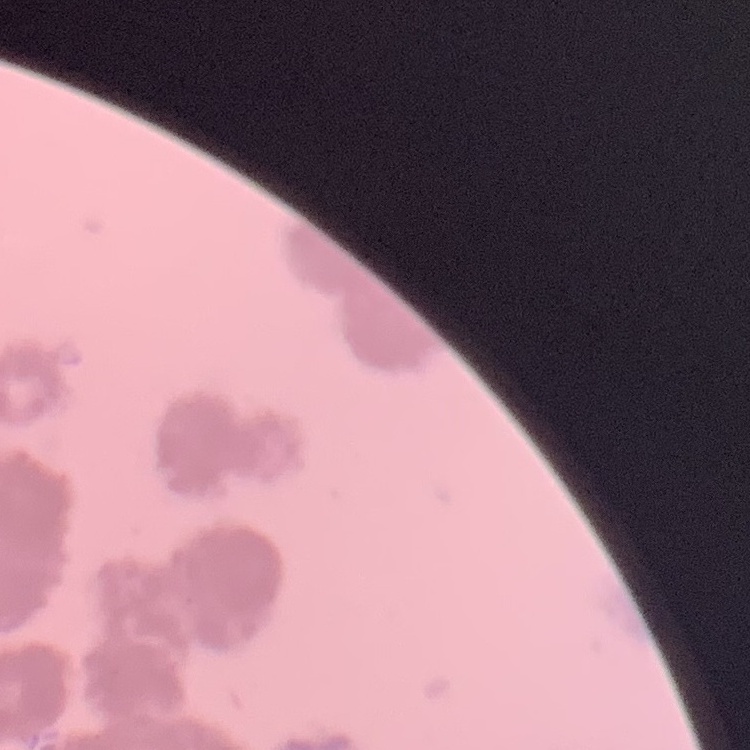

{
  "erythrocyte_morphology": "rouleaux formation",
  "preparation": "thin blood film",
  "image_type": "one tile cut from a larger photomicrograph",
  "stain": "Field's or Giemsa"
}